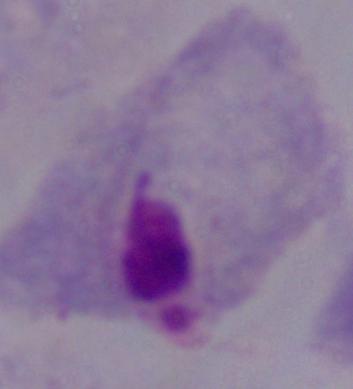

identification = trichomonad
modality = micrograph
magnification = 1000x